Locate every blood parasite and identify its species.
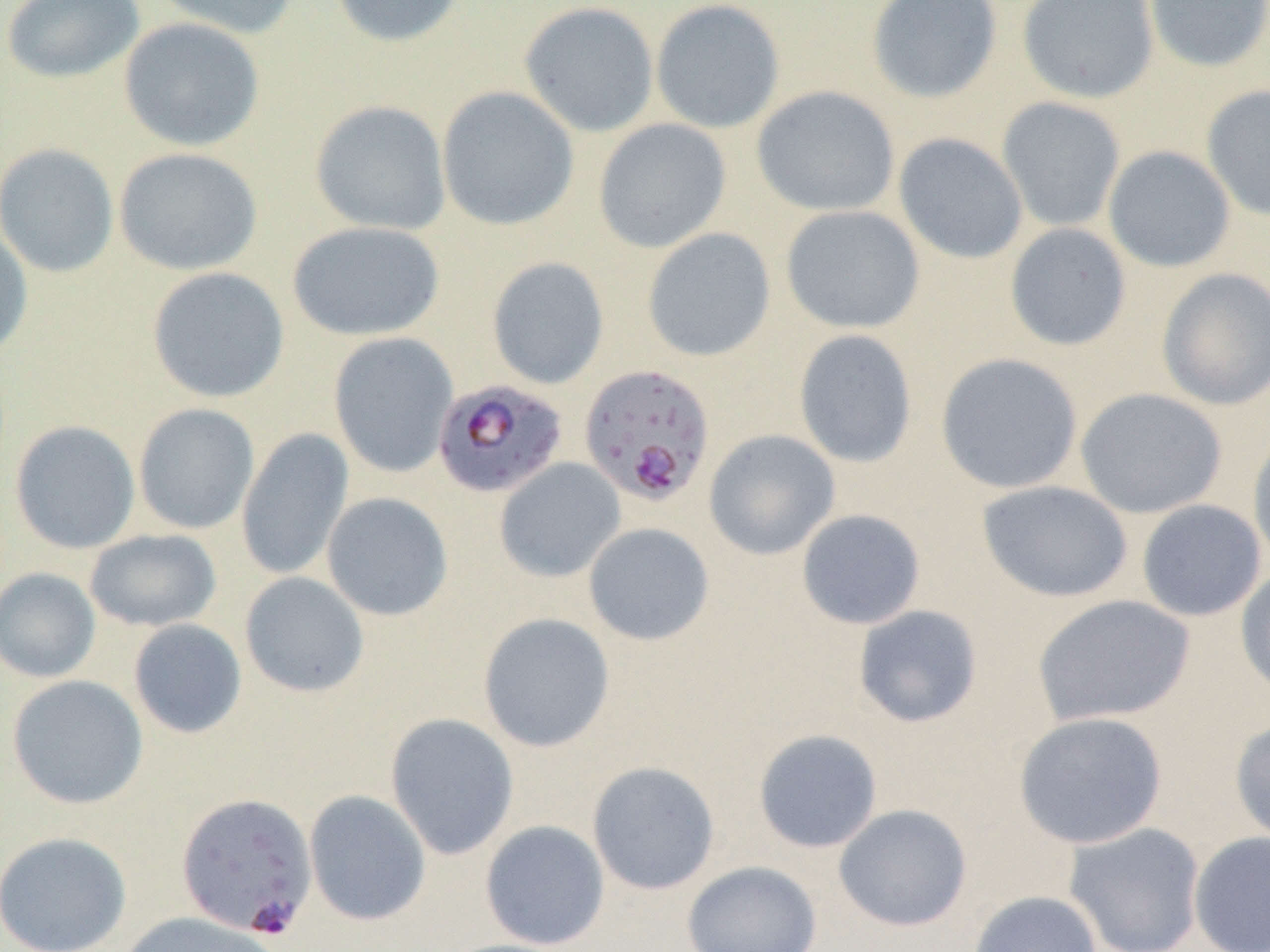

Approximate bounding boxes as [x1, y1, x2, y2] in pixels.
Plasmodium falciparum-infected red blood cells: [579, 363, 715, 507], [433, 379, 568, 498], [176, 792, 318, 939].
No Plasmodium ovale, Plasmodium malariae, Plasmodium vivax, Babesia divergens, or Trypanosoma brucei observed.

slide-level diagnosis = Plasmodium falciparum
uninfected red blood cell locations = approximate bounding boxes as [x1, y1, x2, y2] in pixels: [147, 0, 301, 40], [328, 0, 468, 48], [650, 0, 785, 134], [866, 0, 1003, 105], [1017, 0, 1160, 104], [1144, 0, 1270, 73], [1, 1, 145, 85], [518, 1, 659, 137], [118, 17, 265, 152], [1201, 84, 1270, 221], [436, 85, 580, 231], [751, 85, 900, 217], [996, 97, 1126, 233], [310, 100, 451, 236], [593, 118, 731, 253], [892, 132, 1028, 264], [0, 144, 119, 277], [1103, 145, 1236, 273], [113, 147, 262, 276], [780, 205, 925, 334], [287, 220, 445, 341], [0, 223, 33, 359], [1004, 223, 1132, 351], [641, 227, 777, 362], [487, 257, 609, 389], [146, 266, 290, 403], [1156, 267, 1270, 410], [793, 329, 918, 468], [329, 332, 459, 478], [936, 353, 1083, 494], [1075, 388, 1227, 519], [133, 403, 259, 535], [10, 420, 141, 554], [1247, 424, 1270, 572], [236, 428, 354, 581], [703, 429, 840, 560], [494, 458, 625, 583], [976, 480, 1133, 603], [321, 491, 454, 621], [1136, 499, 1267, 622], [796, 509, 926, 630], [583, 522, 715, 646], [84, 529, 222, 631], [1234, 563, 1270, 700], [0, 567, 101, 683], [240, 571, 370, 697], [1030, 593, 1196, 728], [852, 605, 983, 729], [477, 612, 615, 752], [128, 618, 247, 739], [6, 674, 149, 809], [1013, 711, 1168, 849], [385, 713, 519, 860], [1230, 716, 1270, 848], [753, 728, 883, 853], [587, 761, 720, 895], [304, 789, 431, 925], [833, 803, 972, 932], [479, 820, 610, 950], [1063, 821, 1206, 952], [1188, 830, 1270, 952], [0, 831, 132, 952], [681, 860, 822, 952], [968, 890, 1103, 952], [117, 911, 282, 952], [435, 938, 577, 952]
preparation = thin blood smear
magnification = 1000x
modality = light microscopy
image size = 1270×952 pixels
field of view = one of a larger specimen